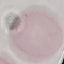 Malaria status: uninfected. Giemsa stain. Thin blood film. Automatically extracted cell patch, resized to 64 × 64 pixels. Acquired by smartphone through the microscope eyepiece.